Point out each Plasmodium parasite.
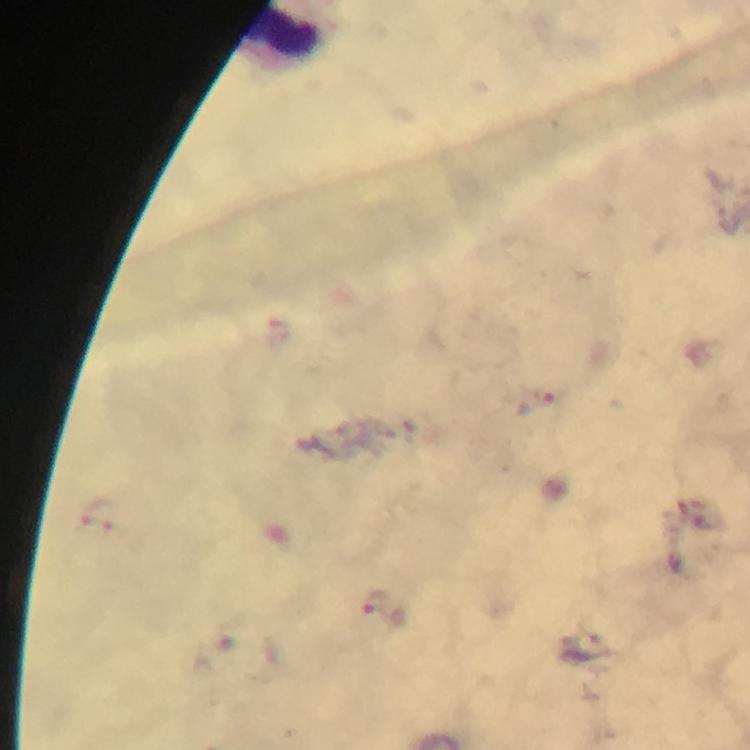

Approximate centers as (x, y) in pixels.
Plasmodium parasites: (277, 333), (546, 400), (102, 514), (375, 603).

{
  "magnification": "100x",
  "cropped_from": "a single field of view",
  "immersion_oil": "applied",
  "capture": "smartphone mounted on the microscope",
  "context": "from a malaria diagnostic workup",
  "stain": "Giemsa",
  "leukocyte_locations": "approximate centers as (x, y) in pixels: (284, 31)",
  "preparation": "thick blood smear",
  "image_size": "750×750 pixels"
}